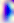
magnification = 400x
identification = Toxoplasma gondii
modality = photomicrograph